Locate and identify every blood parasite.
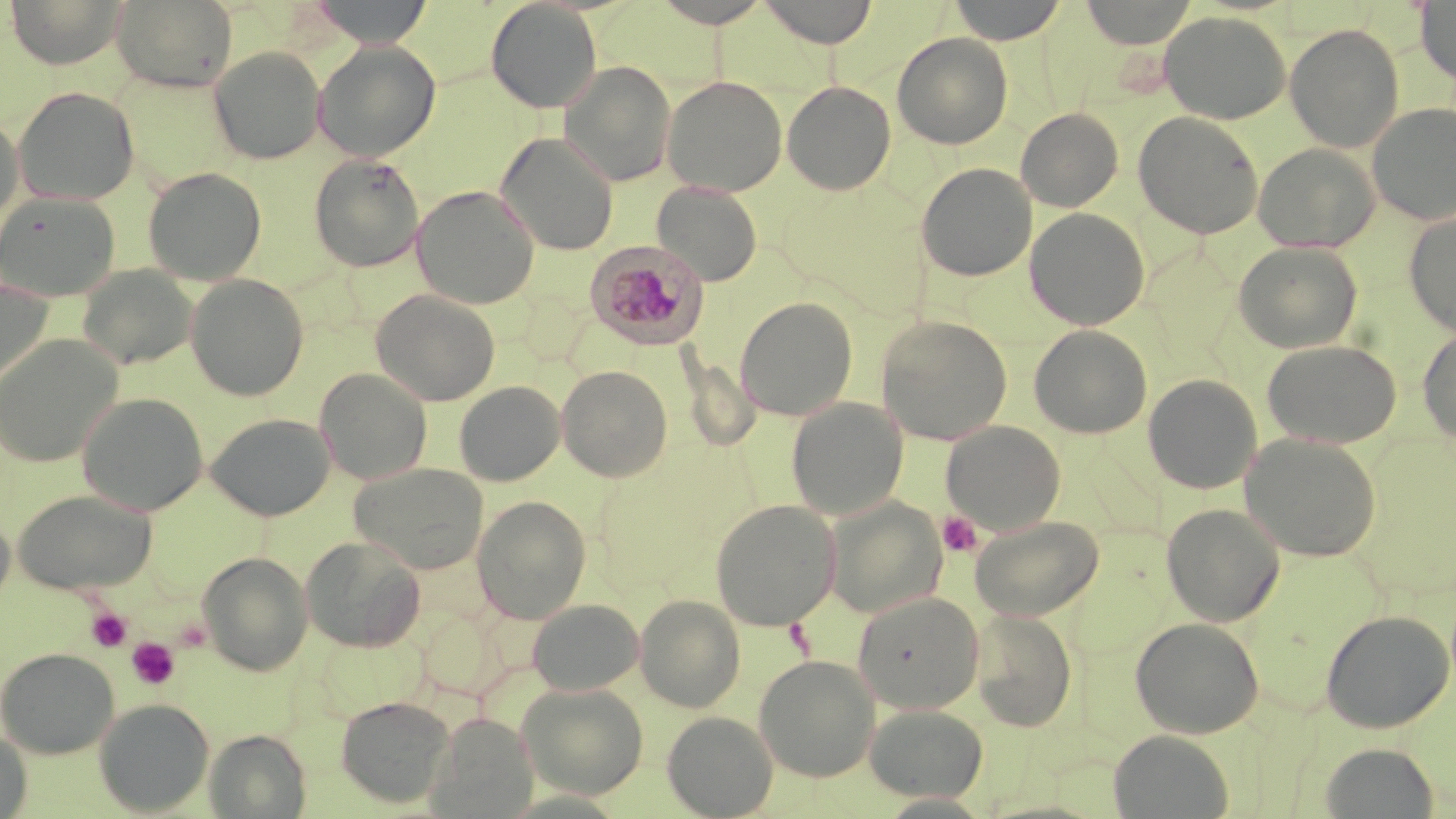

Approximate bounding boxes as [x1, y1, x2, y2] in pixels.
Plasmodium malariae-infected red blood cells: [585, 240, 710, 348].
No Plasmodium falciparum, Plasmodium ovale, Plasmodium vivax, Babesia divergens, or Trypanosoma brucei observed.

slide-level diagnosis = Plasmodium malariae
platelet locations = approximate bounding boxes as [x1, y1, x2, y2] in pixels: [937, 511, 981, 557], [86, 606, 132, 652], [126, 637, 180, 691]
preparation = thin blood smear
magnification = 1000x
modality = light microscopy
image size = 1456×819 pixels
uninfected red blood cell locations = approximate bounding boxes as [x1, y1, x2, y2] in pixels: [4, 0, 127, 68], [111, 0, 238, 92], [310, 0, 434, 47], [485, 0, 602, 113], [651, 0, 774, 28], [757, 0, 879, 47], [947, 0, 1067, 44], [1079, 0, 1199, 48], [1415, 1, 1456, 85], [1159, 10, 1292, 124], [1285, 23, 1405, 152], [892, 33, 1013, 149], [313, 41, 441, 162], [209, 46, 325, 165], [559, 61, 677, 186], [662, 75, 787, 196], [782, 80, 896, 194], [13, 87, 139, 206], [1368, 103, 1456, 224], [1016, 108, 1123, 212], [1133, 112, 1264, 238], [0, 113, 24, 232], [496, 132, 619, 256], [1252, 143, 1380, 253], [309, 153, 425, 272], [916, 162, 1037, 281], [143, 167, 266, 286], [652, 182, 762, 286], [411, 185, 539, 309], [0, 191, 120, 301], [1025, 207, 1150, 330], [1404, 211, 1456, 337], [1233, 241, 1363, 354], [77, 265, 198, 370], [186, 274, 309, 401], [0, 278, 54, 389], [371, 289, 500, 406], [735, 297, 858, 421], [876, 315, 1012, 445], [1029, 324, 1152, 438], [1417, 327, 1456, 447], [0, 334, 123, 468], [1261, 339, 1402, 448], [557, 365, 672, 482], [314, 368, 432, 485], [1143, 374, 1263, 494], [454, 381, 565, 486], [77, 392, 208, 515], [787, 398, 907, 520], [206, 413, 335, 521], [941, 420, 1065, 535], [1240, 433, 1381, 561], [349, 463, 488, 574], [13, 490, 157, 595], [472, 495, 592, 623], [824, 496, 946, 619], [710, 499, 841, 631], [1161, 503, 1285, 626], [0, 508, 15, 610], [968, 516, 1103, 621], [300, 536, 426, 652], [197, 550, 312, 676], [852, 591, 984, 713], [635, 594, 746, 712], [527, 599, 644, 695], [970, 609, 1077, 731], [1320, 609, 1454, 733], [1130, 616, 1264, 738], [0, 647, 120, 759], [754, 654, 880, 781], [517, 683, 649, 800], [335, 695, 454, 808], [94, 698, 214, 816], [864, 704, 988, 802], [430, 711, 538, 817], [662, 711, 778, 818], [0, 729, 32, 819], [205, 729, 311, 819], [1109, 730, 1233, 818], [1319, 742, 1440, 818]
stain = May-Grünwald-Giemsa
field of view = single